State which parasite is depicted.
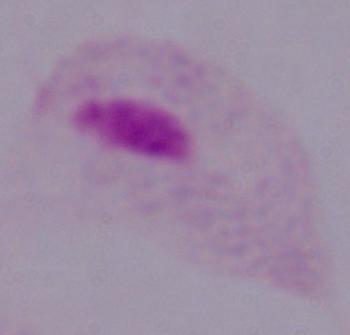

This is a trichomonad.

Summary:
  - Magnification: 1000x
  - Modality: micrograph